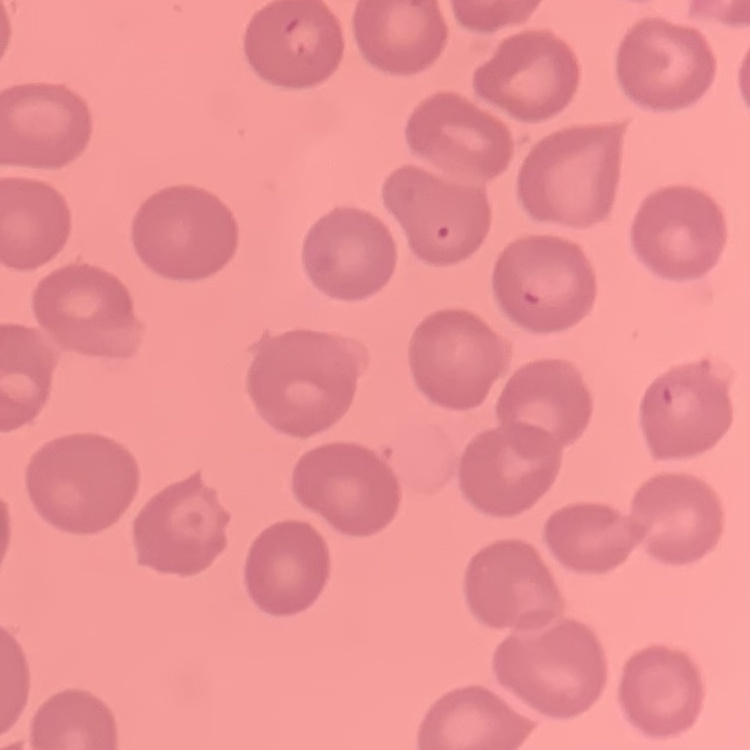
Summary:
  - Erythrocyte morphology: no rouleaux formation
  - Image type: square crop of a larger photomicrograph
  - Stain: Field's or Giemsa
  - Preparation: thin peripheral smear